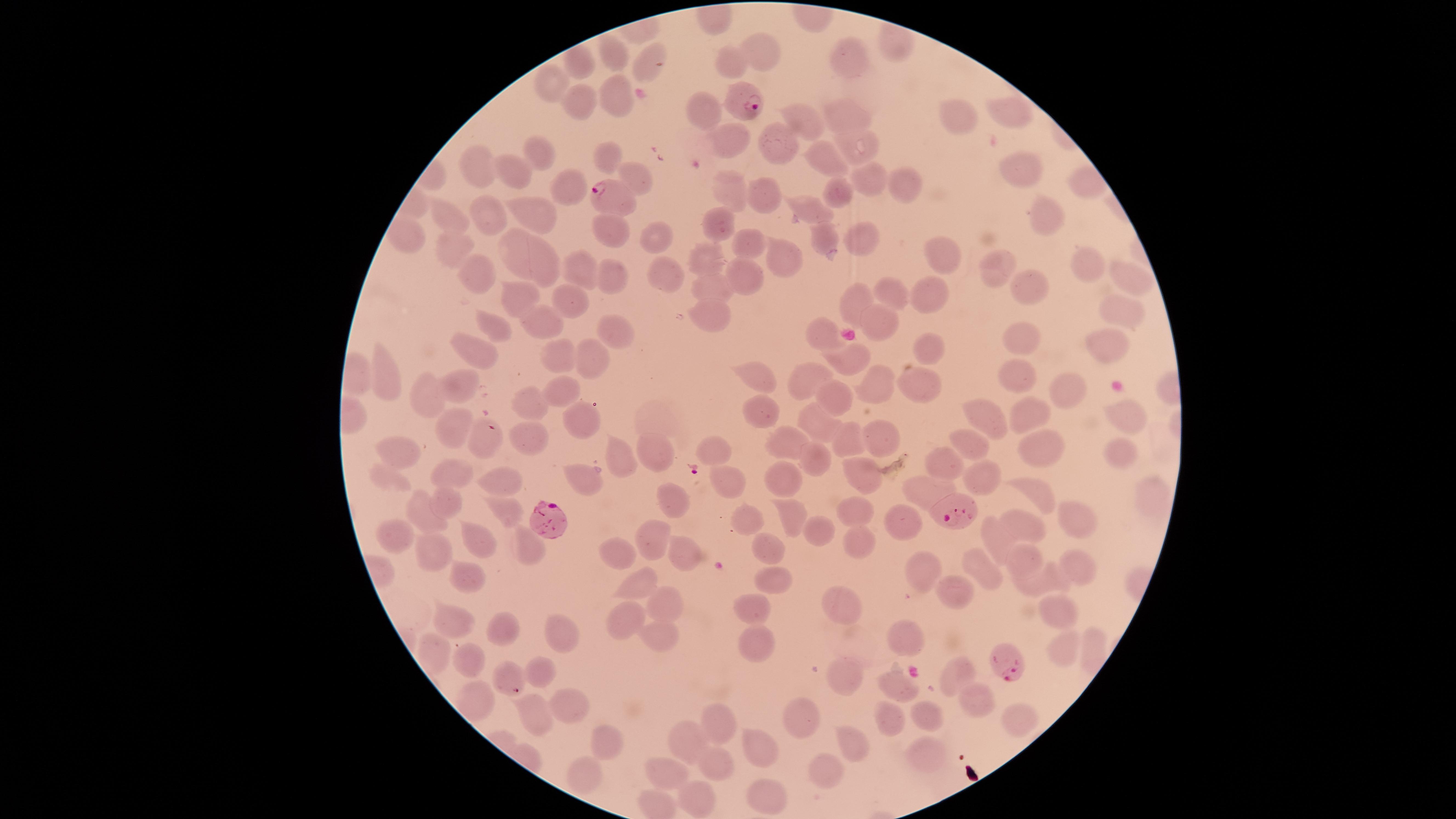
{
  "visible_region": "circular",
  "field_of_view": "single",
  "capture": "smartphone photograph through the microscope eyepiece",
  "presence": "malaria parasites seen",
  "uninfected_red_blood_cells": "approximate marker points, in pixels from the top-left corner: (x=759, y=51), (x=618, y=52), (x=848, y=57), (x=583, y=62), (x=651, y=64), (x=728, y=65), (x=547, y=78), (x=610, y=96), (x=578, y=101), (x=702, y=110), (x=1014, y=110), (x=844, y=112), (x=806, y=116), (x=958, y=119), (x=725, y=134), (x=779, y=142), (x=858, y=148), (x=608, y=153), (x=538, y=156), (x=477, y=162), (x=823, y=164), (x=1017, y=169), (x=514, y=171), (x=631, y=176), (x=872, y=176), (x=572, y=185), (x=901, y=185), (x=843, y=190), (x=729, y=191), (x=761, y=198), (x=812, y=212), (x=442, y=215), (x=491, y=215), (x=538, y=215), (x=1045, y=218), (x=720, y=220), (x=607, y=228), (x=406, y=235), (x=662, y=238), (x=749, y=242), (x=826, y=242), (x=859, y=243), (x=450, y=244), (x=519, y=252), (x=779, y=255), (x=704, y=256), (x=941, y=261), (x=542, y=262), (x=998, y=264), (x=1090, y=264), (x=582, y=271), (x=663, y=273), (x=471, y=274), (x=617, y=274), (x=747, y=277), (x=1134, y=283), (x=715, y=284), (x=1025, y=287), (x=928, y=294), (x=890, y=295), (x=520, y=297), (x=858, y=299), (x=567, y=305), (x=714, y=314), (x=1120, y=314), (x=537, y=320), (x=492, y=325), (x=876, y=325), (x=608, y=331), (x=821, y=334), (x=1021, y=339), (x=1109, y=346), (x=930, y=347), (x=474, y=352), (x=555, y=352), (x=594, y=356), (x=845, y=362), (x=1014, y=369), (x=756, y=374), (x=809, y=374), (x=387, y=381), (x=922, y=385), (x=1059, y=386), (x=872, y=387), (x=462, y=389), (x=562, y=389), (x=430, y=397), (x=842, y=403), (x=529, y=404), (x=764, y=408), (x=578, y=413), (x=1033, y=414), (x=1129, y=414), (x=987, y=417), (x=815, y=424), (x=450, y=427), (x=882, y=435), (x=526, y=436), (x=789, y=440), (x=851, y=442), (x=482, y=445), (x=1038, y=446), (x=717, y=448), (x=971, y=448), (x=400, y=450), (x=618, y=450), (x=1116, y=454), (x=655, y=455), (x=814, y=458), (x=944, y=459), (x=455, y=474), (x=855, y=474), (x=979, y=475), (x=385, y=479), (x=584, y=479), (x=731, y=480), (x=779, y=481), (x=505, y=482), (x=1037, y=493), (x=927, y=494), (x=669, y=497), (x=451, y=502), (x=506, y=510), (x=791, y=512), (x=860, y=512), (x=425, y=514), (x=1079, y=517), (x=753, y=521), (x=907, y=522), (x=1030, y=525), (x=820, y=532), (x=397, y=535), (x=653, y=535), (x=995, y=537), (x=478, y=540), (x=529, y=541), (x=859, y=544), (x=761, y=546), (x=687, y=550), (x=616, y=555), (x=438, y=556), (x=1018, y=560), (x=977, y=562), (x=1075, y=564), (x=920, y=569), (x=469, y=579), (x=770, y=580), (x=639, y=585), (x=1035, y=585), (x=960, y=593), (x=754, y=603), (x=660, y=604), (x=845, y=607), (x=1060, y=615), (x=631, y=618), (x=455, y=626), (x=505, y=631), (x=911, y=635), (x=659, y=636), (x=556, y=637), (x=752, y=640), (x=1058, y=643), (x=466, y=662), (x=507, y=670), (x=540, y=670), (x=960, y=670), (x=846, y=676), (x=898, y=685), (x=973, y=700), (x=476, y=701), (x=574, y=705), (x=533, y=713), (x=929, y=714), (x=804, y=720), (x=890, y=721), (x=717, y=722), (x=1021, y=722), (x=852, y=738), (x=695, y=741), (x=607, y=742), (x=765, y=747), (x=925, y=754), (x=715, y=761), (x=826, y=768), (x=669, y=772), (x=588, y=779), (x=769, y=794), (x=698, y=801)",
  "stain": "Giemsa",
  "parasitized_red_blood_cells": "approximate marker points, in pixels from the top-left corner: (x=742, y=94), (x=612, y=196), (x=958, y=500), (x=552, y=522), (x=1004, y=655)",
  "image_size": "1456×819 pixels",
  "species": "Plasmodium falciparum",
  "preparation": "thin blood film"
}